Comment on the morphology of the red blood cells.
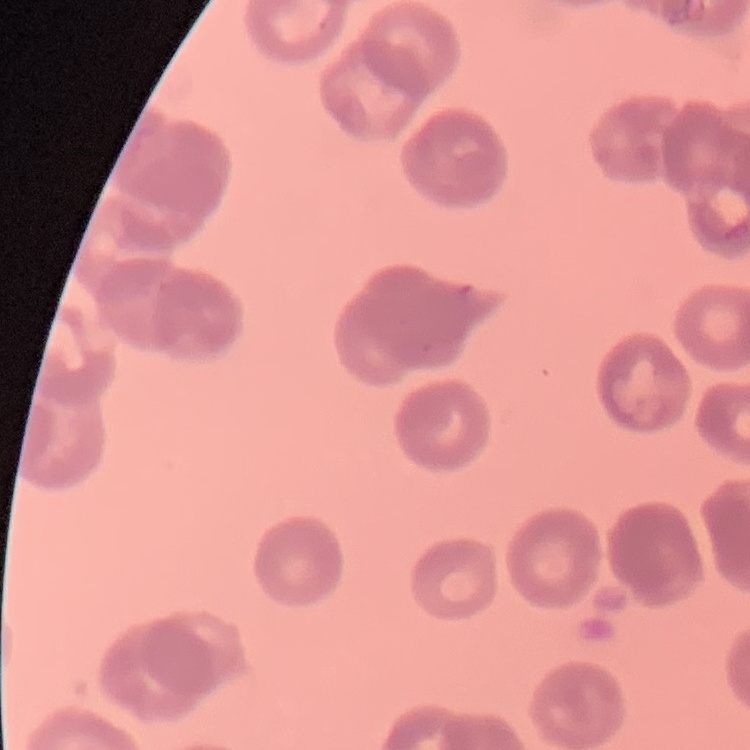

They show rouleaux formation.

Square crop of a larger photomicrograph. Thin blood film. Field's or Giemsa stain.